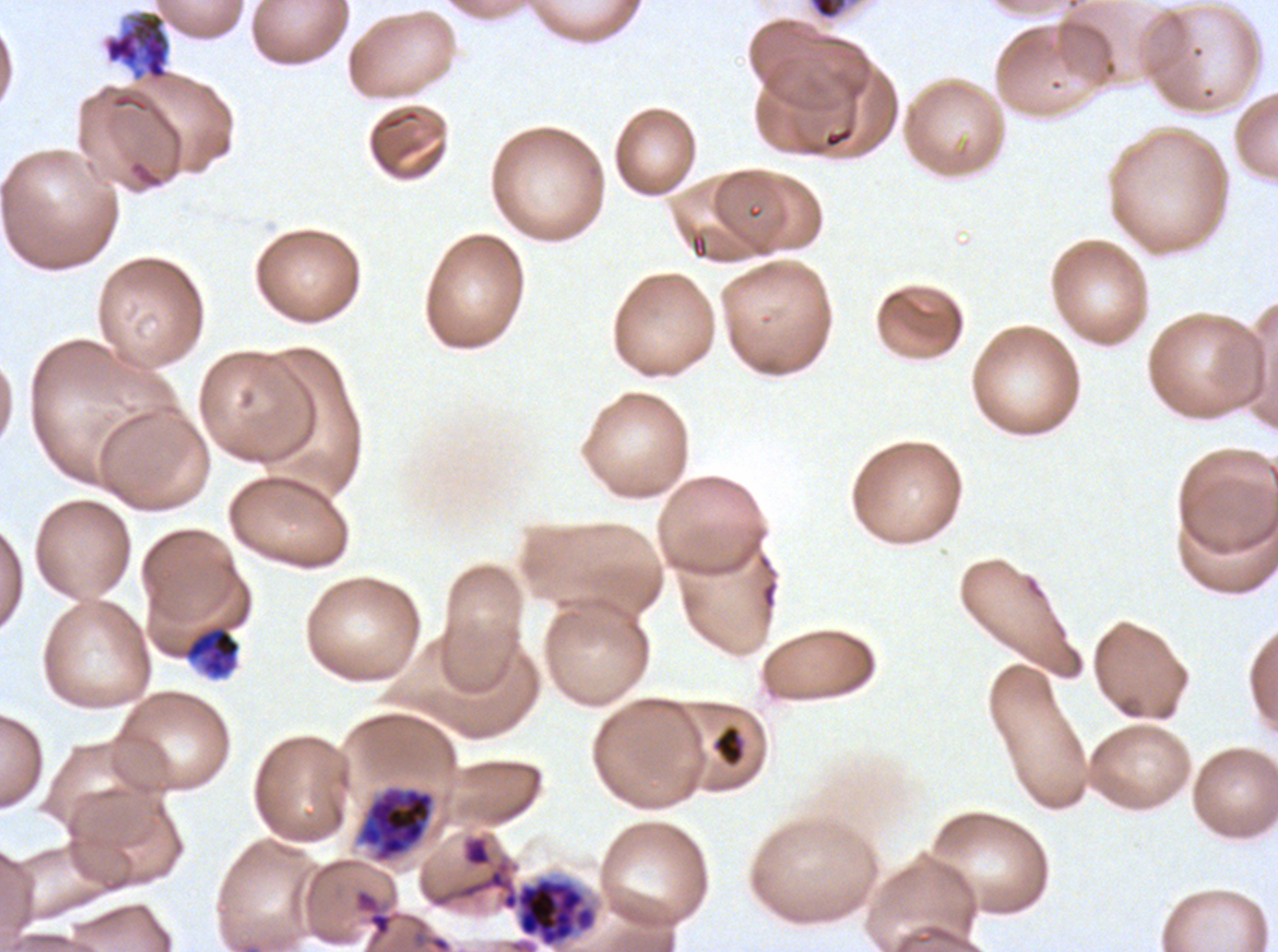
notation = approximate bounding boxes as (x1, y1, x2, y2) in pixels
late schizont locations = (809, 0, 847, 19)
segmenter locations = (501, 877, 596, 946)
debris locations = (185, 626, 240, 678), (711, 724, 745, 768)
early schizont locations = (104, 12, 170, 80), (357, 786, 436, 863)
field of view = sub-image separated from a larger composite
life-cycle stages observed = early schizont, late schizont, segmenter
image size = 1278×952 pixels
preparation = thin blood smear
specimen = P. falciparum cultured ex vivo for 24 to 48 hours, from a patient in The Gambia
stain = Giemsa